Report the malaria status of this cell.
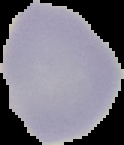

Uninfected.

Summary:
  - Image size: 124×145 pixels
  - Preparation: thin blood smear
  - Image type: segmented cell region with the area outside set to black